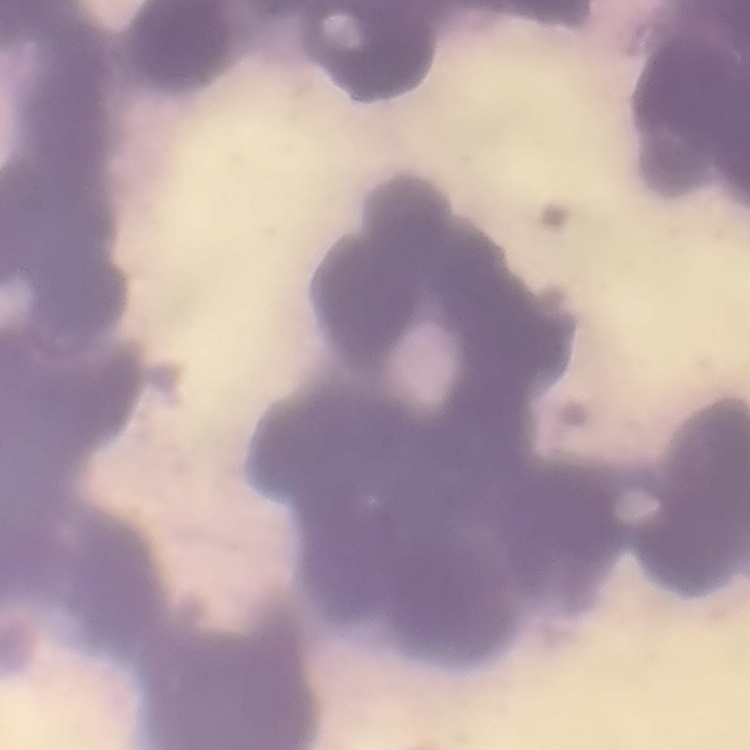 The erythrocytes show rouleaux formation. Thin blood smear. One tile cut from a larger photomicrograph. Field's or Giemsa stain.